Outline each Trypanosoma brucei.
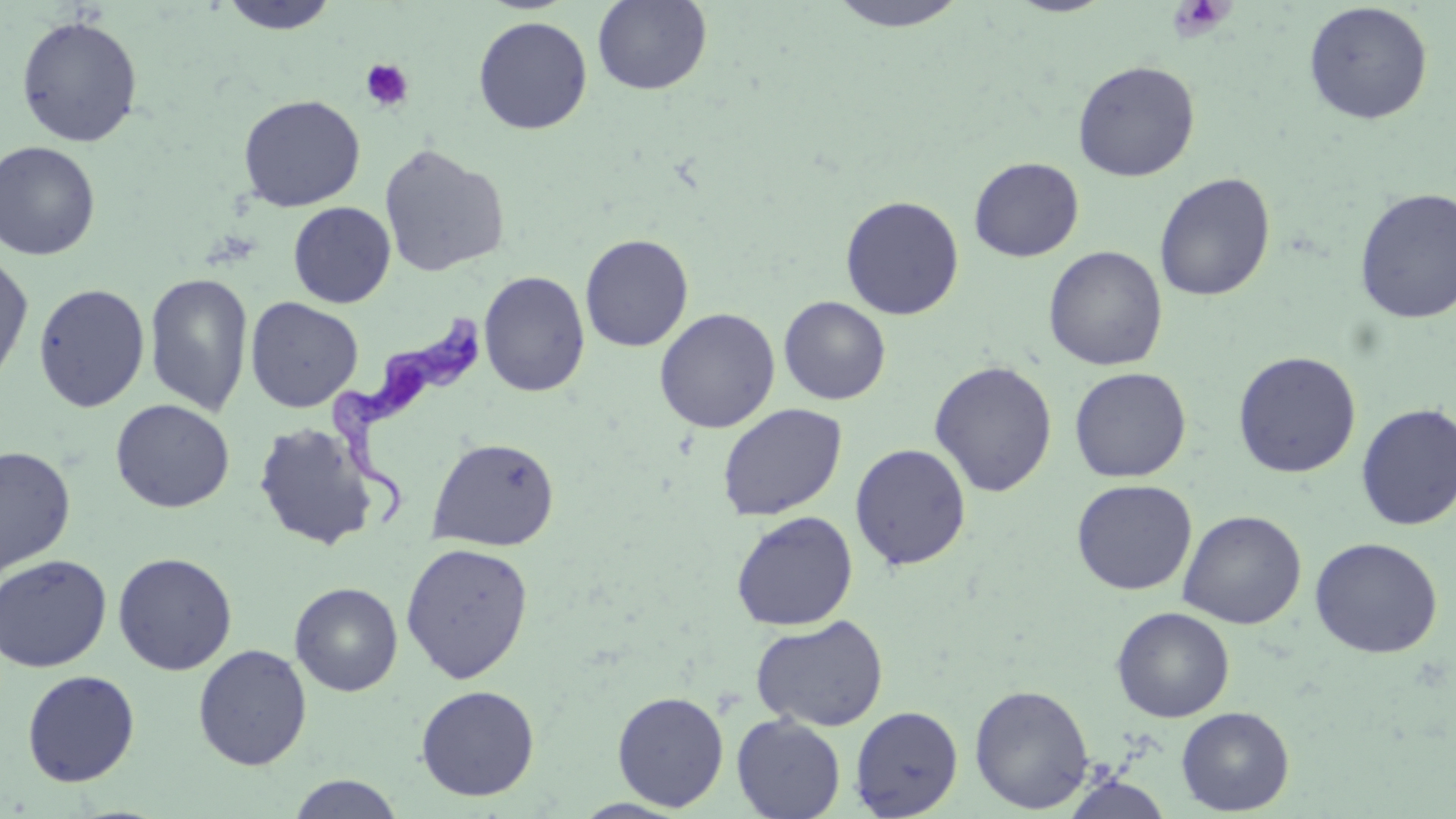

Approximate bounding boxes as named x1/y1/x2/y2 corners in pixels.
Trypanosoma brucei: (x1=325, y1=304, x2=487, y2=531).

slide_level_diagnosis: Trypanosoma brucei
magnification: 1000x
preparation: thin blood film
platelet_locations: 'approximate bounding boxes as named x1/y1/x2/y2 corners in pixels: (x1=1166, y1=0, x2=1235, y2=42), (x1=359, y1=58, x2=415, y2=113)'
modality: optical microscopy
field_of_view: single
uninfected_red_blood_cell_locations: 'approximate bounding boxes as named x1/y1/x2/y2 corners in pixels: (x1=216, y1=0, x2=343, y2=35), (x1=824, y1=0, x2=971, y2=32), (x1=592, y1=1, x2=712, y2=95), (x1=1303, y1=2, x2=1433, y2=125), (x1=15, y1=14, x2=144, y2=147), (x1=473, y1=16, x2=593, y2=134), (x1=1072, y1=60, x2=1200, y2=181), (x1=238, y1=94, x2=365, y2=212), (x1=0, y1=140, x2=101, y2=261), (x1=378, y1=143, x2=509, y2=277), (x1=968, y1=157, x2=1084, y2=261), (x1=1154, y1=172, x2=1275, y2=302), (x1=1353, y1=187, x2=1456, y2=325), (x1=840, y1=195, x2=964, y2=320), (x1=288, y1=201, x2=396, y2=308), (x1=579, y1=233, x2=694, y2=352), (x1=1043, y1=245, x2=1168, y2=371), (x1=0, y1=252, x2=34, y2=390), (x1=478, y1=270, x2=590, y2=397), (x1=144, y1=271, x2=253, y2=417), (x1=33, y1=283, x2=150, y2=413), (x1=778, y1=296, x2=891, y2=405), (x1=245, y1=297, x2=363, y2=412), (x1=654, y1=308, x2=780, y2=433), (x1=1232, y1=351, x2=1362, y2=478), (x1=929, y1=360, x2=1057, y2=497), (x1=1069, y1=366, x2=1191, y2=483), (x1=110, y1=399, x2=235, y2=513), (x1=716, y1=403, x2=847, y2=521), (x1=1355, y1=403, x2=1456, y2=531), (x1=253, y1=421, x2=380, y2=551), (x1=426, y1=436, x2=560, y2=551), (x1=849, y1=443, x2=972, y2=570), (x1=0, y1=445, x2=76, y2=577), (x1=1071, y1=479, x2=1197, y2=595), (x1=1177, y1=509, x2=1306, y2=629), (x1=731, y1=511, x2=858, y2=631), (x1=1310, y1=537, x2=1443, y2=658), (x1=400, y1=541, x2=534, y2=684), (x1=113, y1=552, x2=238, y2=675), (x1=0, y1=553, x2=113, y2=672), (x1=289, y1=582, x2=403, y2=696), (x1=1111, y1=606, x2=1234, y2=722), (x1=750, y1=615, x2=889, y2=732), (x1=193, y1=643, x2=312, y2=770), (x1=21, y1=670, x2=140, y2=787), (x1=970, y1=683, x2=1095, y2=813), (x1=415, y1=684, x2=540, y2=801), (x1=612, y1=690, x2=729, y2=811), (x1=850, y1=705, x2=963, y2=818), (x1=1176, y1=706, x2=1294, y2=815), (x1=731, y1=714, x2=846, y2=819), (x1=287, y1=774, x2=405, y2=818), (x1=1061, y1=774, x2=1174, y2=818)'
image_size: 1456×819 pixels
stain: May-Grünwald-Giemsa